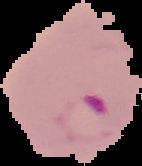
Summary:
  - Image type: segmented cell region on a black background
  - Malaria status: parasitized
  - Image size: 142×166 pixels
  - Preparation: thin blood smear